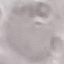

Summary:
  - Malaria status: uninfected
  - Preparation: thin smear
  - Capture: smartphone through the microscope eyepiece
  - Stain: Giemsa
  - Image type: cell patch, automatically extracted from a larger field of view and resized to 64 × 64 pixels